Assess this cell for malaria.
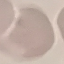
Uninfected.

Summary:
  - Preparation: thin smear
  - Stain: Giemsa
  - Image type: cell patch, automatically extracted from a larger field of view and resized to 64 × 64 pixels
  - Capture: smartphone through the microscope eyepiece